Locate every blood parasite and identify its species.
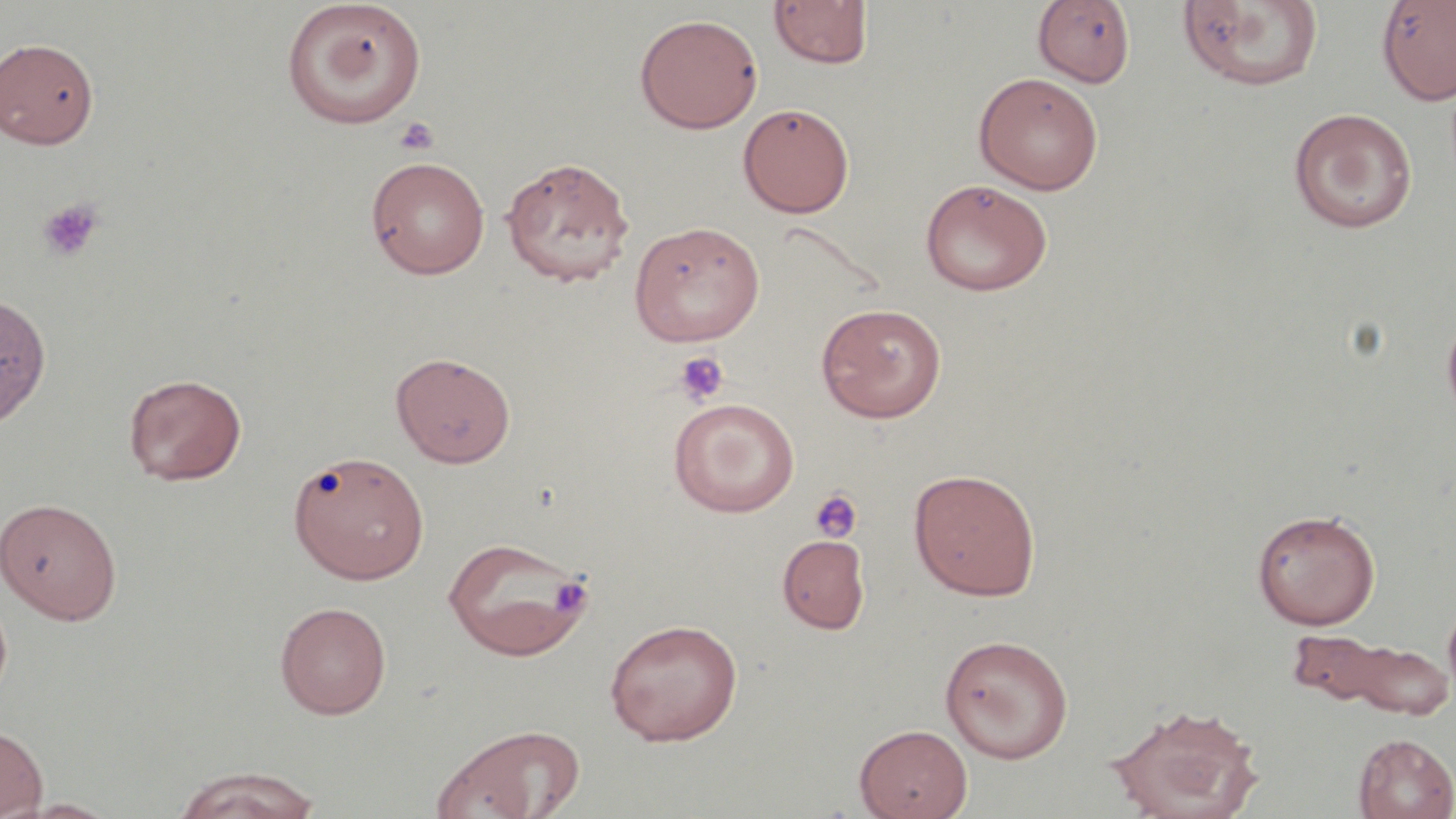
No blood parasites observed.

Approximate bounding boxes as named x1/y1/x2/y2 corners in pixels. Uninfected red blood cell locations: (x1=1177, y1=0, x2=1325, y2=93), (x1=1376, y1=0, x2=1456, y2=106), (x1=280, y1=1, x2=428, y2=129), (x1=767, y1=1, x2=873, y2=71), (x1=1032, y1=1, x2=1136, y2=88), (x1=634, y1=13, x2=763, y2=134), (x1=0, y1=37, x2=99, y2=149), (x1=973, y1=71, x2=1104, y2=195), (x1=738, y1=103, x2=855, y2=217), (x1=1287, y1=108, x2=1418, y2=233), (x1=365, y1=155, x2=491, y2=279), (x1=500, y1=155, x2=635, y2=287), (x1=920, y1=178, x2=1053, y2=296), (x1=627, y1=220, x2=765, y2=346), (x1=0, y1=293, x2=52, y2=428), (x1=816, y1=302, x2=947, y2=422), (x1=1441, y1=304, x2=1456, y2=431), (x1=390, y1=352, x2=516, y2=468), (x1=123, y1=373, x2=247, y2=485), (x1=668, y1=397, x2=800, y2=517), (x1=288, y1=449, x2=430, y2=584), (x1=908, y1=468, x2=1042, y2=601), (x1=0, y1=497, x2=123, y2=624), (x1=1251, y1=508, x2=1380, y2=630), (x1=776, y1=533, x2=872, y2=634), (x1=441, y1=535, x2=593, y2=660), (x1=1443, y1=599, x2=1456, y2=704), (x1=274, y1=601, x2=392, y2=719), (x1=604, y1=618, x2=743, y2=746), (x1=939, y1=633, x2=1074, y2=763), (x1=1293, y1=633, x2=1455, y2=719), (x1=1107, y1=701, x2=1265, y2=819), (x1=0, y1=723, x2=49, y2=819), (x1=854, y1=723, x2=973, y2=819), (x1=432, y1=724, x2=584, y2=819), (x1=1353, y1=733, x2=1456, y2=818), (x1=172, y1=766, x2=322, y2=819), (x1=11, y1=798, x2=125, y2=818). Platelet locations: (x1=395, y1=117, x2=439, y2=156), (x1=37, y1=198, x2=104, y2=263), (x1=673, y1=350, x2=730, y2=407), (x1=810, y1=489, x2=863, y2=543), (x1=549, y1=575, x2=593, y2=616). Slide-level diagnosis: no evidence of blood parasites. Image is 1456×819 pixels. Thin blood smear. One field of a larger specimen. 1000x magnification. May-Grünwald-Giemsa-stained preparation. Optical microscopy.